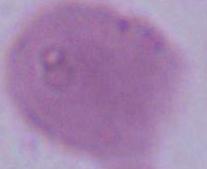

Photomicrograph. A red blood cell is shown. Captured at 1000x magnification.